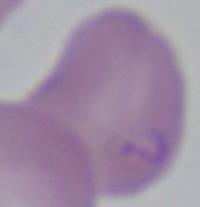

modality = photomicrograph
magnification = 1000x
identification = Babesia